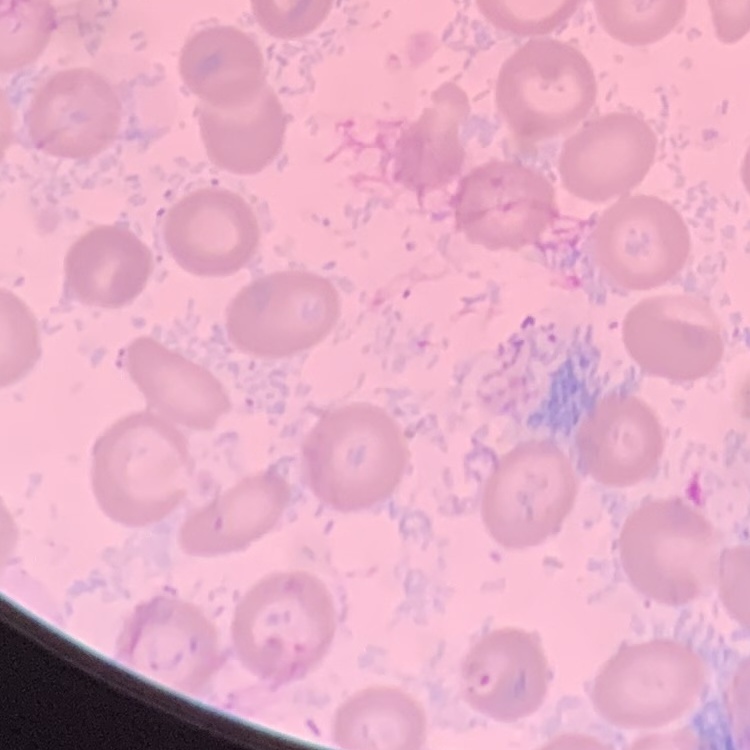

Summary:
  - Red blood cell morphology: no rouleaux formation
  - Preparation: thin blood smear
  - Image type: square crop of a larger photomicrograph
  - Stain: Field's or Giemsa